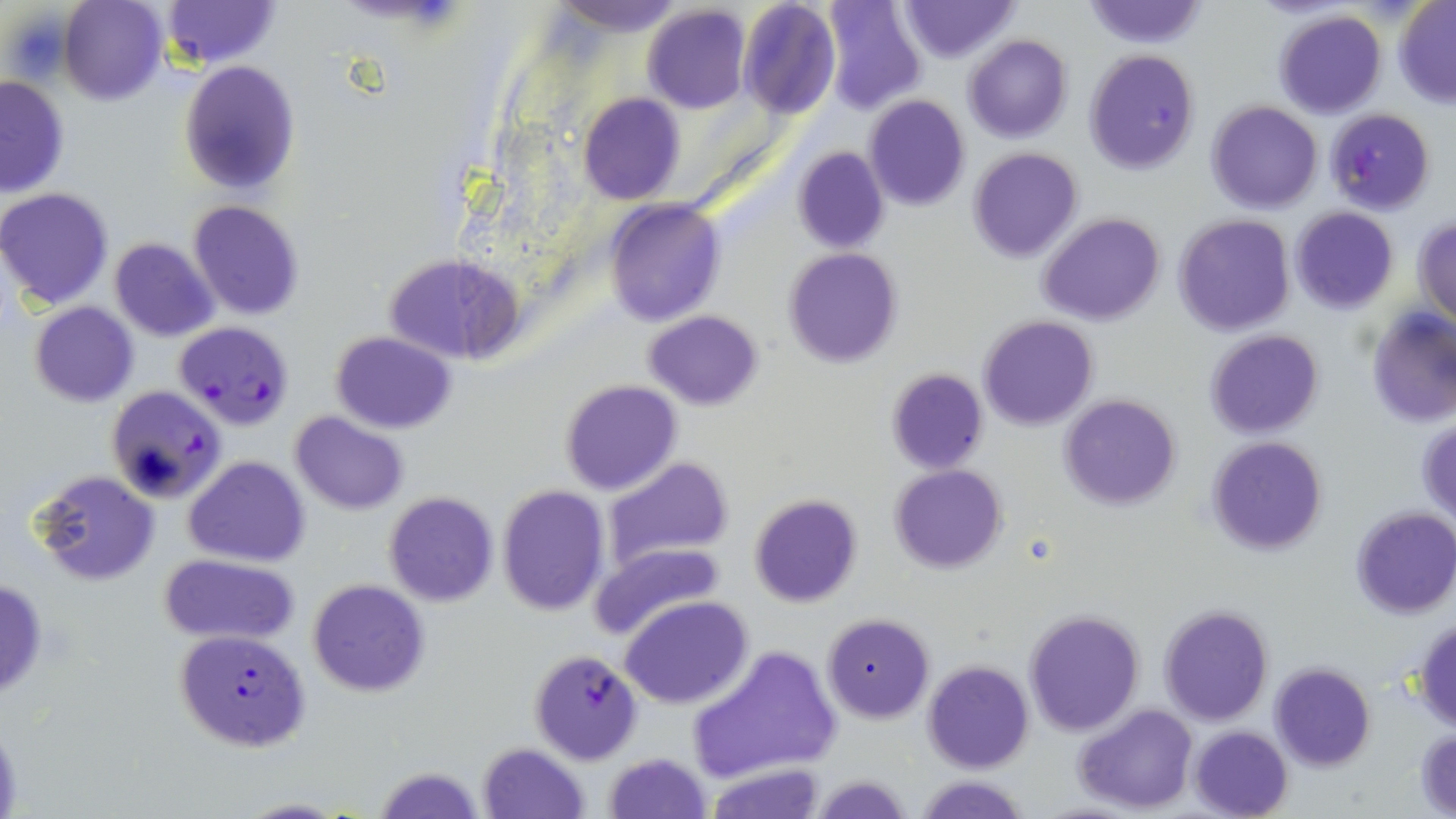

{
  "slide_level_diagnosis": "Plasmodium falciparum",
  "field_of_view": "single",
  "image_size": "1456×819 pixels",
  "modality": "light microscopy",
  "uninfected_red_blood_cell_locations": "approximate bounding boxes as named x1/y1/x2/y2 corners in pixels: (x1=60, y1=0, x2=167, y2=106), (x1=161, y1=0, x2=279, y2=69), (x1=551, y1=0, x2=683, y2=38), (x1=819, y1=0, x2=926, y2=116), (x1=897, y1=0, x2=1019, y2=64), (x1=1081, y1=0, x2=1208, y2=48), (x1=737, y1=1, x2=841, y2=120), (x1=1393, y1=1, x2=1456, y2=107), (x1=643, y1=6, x2=750, y2=114), (x1=1273, y1=10, x2=1387, y2=118), (x1=963, y1=34, x2=1072, y2=143), (x1=1084, y1=49, x2=1200, y2=173), (x1=179, y1=60, x2=301, y2=197), (x1=0, y1=75, x2=70, y2=197), (x1=578, y1=94, x2=684, y2=205), (x1=864, y1=96, x2=970, y2=210), (x1=1208, y1=101, x2=1324, y2=214), (x1=792, y1=145, x2=889, y2=255), (x1=968, y1=148, x2=1082, y2=263), (x1=0, y1=187, x2=115, y2=311), (x1=604, y1=199, x2=725, y2=326), (x1=189, y1=200, x2=303, y2=320), (x1=1289, y1=207, x2=1398, y2=313), (x1=1037, y1=213, x2=1166, y2=327), (x1=1174, y1=215, x2=1293, y2=336), (x1=1413, y1=217, x2=1456, y2=323), (x1=110, y1=238, x2=220, y2=342), (x1=783, y1=247, x2=902, y2=367), (x1=386, y1=253, x2=523, y2=364), (x1=30, y1=302, x2=138, y2=408), (x1=644, y1=310, x2=764, y2=409), (x1=1366, y1=310, x2=1456, y2=429), (x1=978, y1=316, x2=1098, y2=430), (x1=1204, y1=329, x2=1325, y2=438), (x1=329, y1=331, x2=457, y2=434), (x1=885, y1=368, x2=989, y2=474), (x1=560, y1=380, x2=682, y2=497), (x1=1058, y1=394, x2=1182, y2=510), (x1=289, y1=412, x2=409, y2=515), (x1=1418, y1=417, x2=1456, y2=522), (x1=1206, y1=436, x2=1328, y2=554), (x1=183, y1=455, x2=311, y2=568), (x1=603, y1=458, x2=732, y2=571), (x1=890, y1=464, x2=1008, y2=573), (x1=32, y1=470, x2=160, y2=587), (x1=497, y1=485, x2=609, y2=615), (x1=383, y1=492, x2=499, y2=608), (x1=750, y1=495, x2=862, y2=607), (x1=1351, y1=506, x2=1456, y2=620), (x1=588, y1=543, x2=726, y2=640), (x1=158, y1=554, x2=301, y2=646), (x1=0, y1=576, x2=48, y2=702), (x1=307, y1=578, x2=430, y2=697), (x1=619, y1=597, x2=753, y2=710), (x1=1159, y1=604, x2=1272, y2=725), (x1=1024, y1=609, x2=1144, y2=735), (x1=822, y1=613, x2=935, y2=722), (x1=1412, y1=616, x2=1456, y2=731), (x1=689, y1=646, x2=843, y2=781), (x1=923, y1=660, x2=1034, y2=773), (x1=1270, y1=663, x2=1376, y2=771), (x1=1074, y1=704, x2=1198, y2=815), (x1=0, y1=721, x2=22, y2=813), (x1=1190, y1=726, x2=1292, y2=818), (x1=1414, y1=728, x2=1456, y2=814), (x1=478, y1=742, x2=588, y2=819), (x1=604, y1=752, x2=712, y2=819), (x1=706, y1=764, x2=828, y2=819), (x1=374, y1=766, x2=484, y2=819), (x1=811, y1=774, x2=914, y2=818), (x1=918, y1=775, x2=1029, y2=818), (x1=232, y1=797, x2=347, y2=818)",
  "stain": "May-Grünwald-Giemsa",
  "magnification": "1000x",
  "preparation": "thin blood smear",
  "plasmodium_falciparum_infected_red_blood_cell_locations": "approximate bounding boxes as named x1/y1/x2/y2 corners in pixels: (x1=1325, y1=109, x2=1434, y2=215), (x1=174, y1=321, x2=294, y2=428), (x1=107, y1=387, x2=225, y2=504), (x1=175, y1=630, x2=311, y2=750), (x1=528, y1=649, x2=644, y2=764)"
}